Describe the morphology of the erythrocytes.
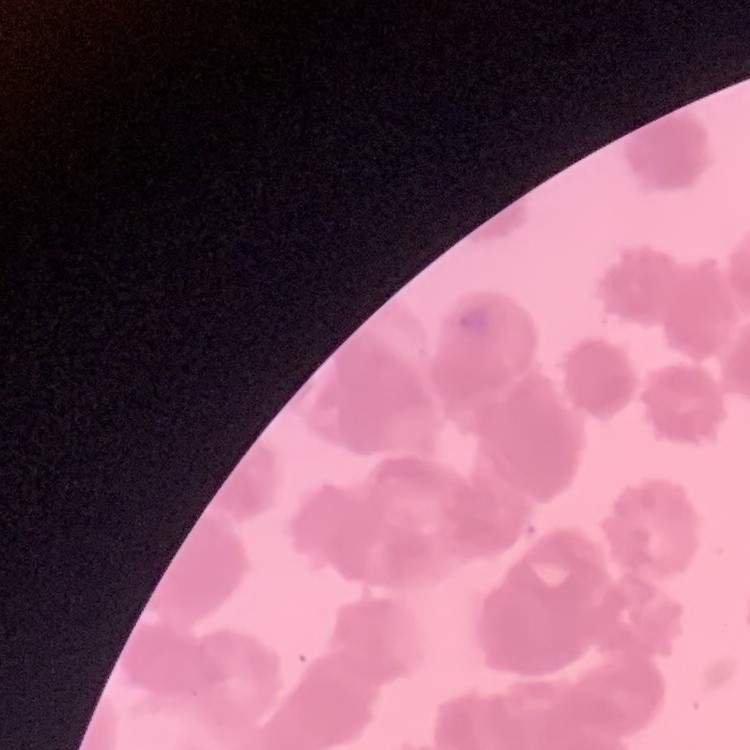
They show rouleaux formation.

One tile cut from a larger photomicrograph. Field's or Giemsa stain. Thin blood film.